Assess this cell for malaria.
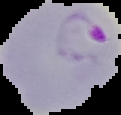
Parasitized.

preparation = thin blood smear
image type = cell region segmented out of the field of view; surrounding area masked to black
image size = 121×115 pixels